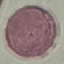

Malaria status: uninfected. Photographed with a smartphone camera at the microscope eyepiece. Giemsa-stained preparation. Thin smear of blood. Cell patch, automatically extracted from a larger field of view and resized to 64 × 64 pixels.